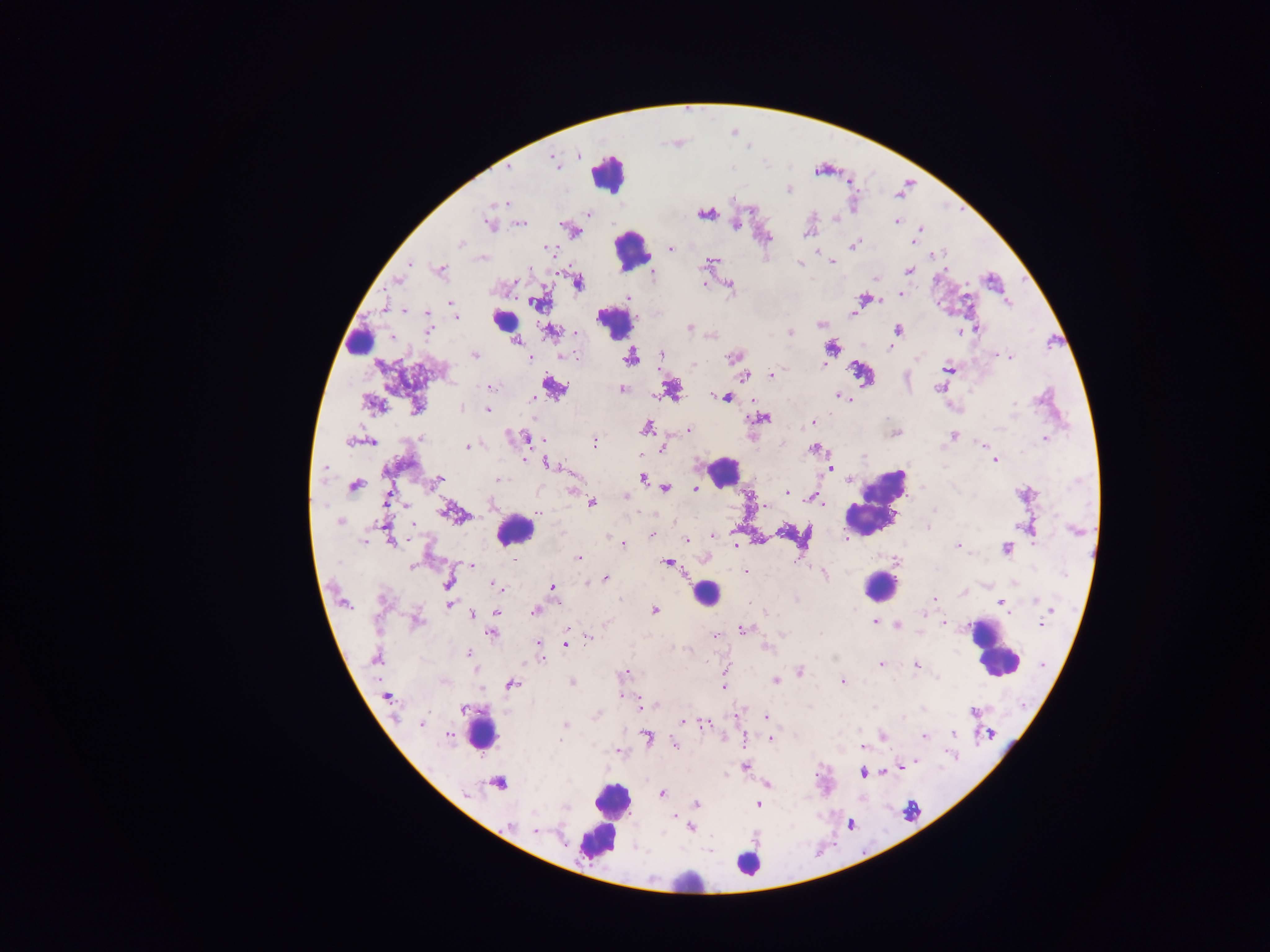

{
  "field_of_view": "single",
  "country": "Ghana",
  "image_size": "1270×952 pixels",
  "leukocyte_locations": "approximate centers as [x, y] in pixels: [608, 172], [630, 249], [503, 320], [613, 322], [359, 341], [723, 471], [873, 502], [514, 530], [879, 586], [706, 593], [992, 648], [482, 733], [610, 807], [596, 839], [747, 864], [685, 887]",
  "plasmodium_parasite_locations": "approximate centers as [x, y] in pixels: [555, 162], [509, 167], [788, 189], [506, 203], [705, 213], [587, 214], [897, 222], [489, 224], [520, 224], [736, 224], [920, 229], [806, 234], [914, 240], [459, 244], [853, 245], [548, 248], [670, 249], [816, 252], [932, 255], [483, 258], [708, 262], [832, 262], [410, 263], [799, 264], [530, 269], [440, 270], [909, 270], [652, 273], [874, 278], [397, 280], [578, 282], [704, 284], [730, 286], [901, 294], [628, 298], [862, 298], [1007, 301], [451, 303], [536, 303], [855, 309], [404, 310], [427, 313], [853, 314], [456, 317], [821, 324], [690, 327], [429, 330], [897, 330], [977, 330], [550, 331], [959, 332], [577, 333], [790, 333], [516, 341], [831, 348], [890, 348], [662, 354], [474, 355], [997, 355], [568, 356], [630, 357], [732, 357], [1010, 357], [529, 358], [917, 359], [694, 365], [823, 365], [949, 368], [772, 374], [744, 375], [553, 387], [491, 388], [622, 389], [672, 389], [938, 389], [838, 396], [727, 397], [534, 399], [373, 404], [1014, 405], [417, 406], [462, 408], [488, 409], [765, 417], [812, 423], [647, 427], [689, 430], [896, 433], [420, 437], [953, 437], [526, 438], [1045, 438], [543, 440], [351, 441], [368, 441], [595, 442], [980, 444], [467, 446], [663, 448], [814, 449], [864, 457], [995, 460], [547, 464], [325, 469], [830, 469], [439, 478], [644, 479], [498, 480], [354, 485], [665, 488], [695, 488], [786, 492], [750, 495], [625, 497], [817, 497], [387, 498], [592, 502], [820, 502], [765, 505], [934, 510], [450, 512], [538, 513], [339, 522], [412, 524], [928, 527], [1075, 530], [652, 535], [712, 536], [363, 541], [686, 541], [391, 542], [623, 543], [957, 544], [736, 545], [1006, 549], [578, 557], [512, 561], [796, 561], [668, 563], [470, 565], [413, 568], [746, 572], [825, 574], [606, 578], [587, 582], [448, 584], [492, 584], [551, 587], [963, 593], [934, 599], [1037, 600], [797, 601], [1000, 603], [449, 604], [536, 610], [654, 610], [1051, 610], [496, 612], [473, 614], [418, 621], [875, 622], [944, 623], [1041, 623], [896, 625], [567, 628], [743, 629], [491, 633], [782, 634], [566, 635], [715, 636], [589, 639], [538, 643], [566, 643], [765, 649], [469, 653], [540, 656], [376, 658], [881, 664], [916, 666], [799, 672], [622, 674], [780, 679], [776, 680], [843, 682], [572, 683], [512, 685], [725, 687], [622, 696], [387, 697], [639, 704], [645, 705], [652, 705], [463, 709], [974, 712], [598, 715], [766, 716], [902, 718], [683, 721], [422, 723], [565, 724], [704, 725], [954, 733], [449, 735], [883, 737], [924, 737], [647, 738], [770, 738], [559, 740], [743, 740], [675, 744], [862, 746], [618, 752], [916, 762], [901, 766], [745, 767], [863, 772], [884, 772], [498, 783], [768, 784], [466, 793], [662, 794], [697, 804], [758, 805], [567, 808], [674, 817], [509, 825], [691, 827], [536, 831]",
  "preparation": "thick blood film",
  "capture": "mobile-phone photograph through a microscope"
}